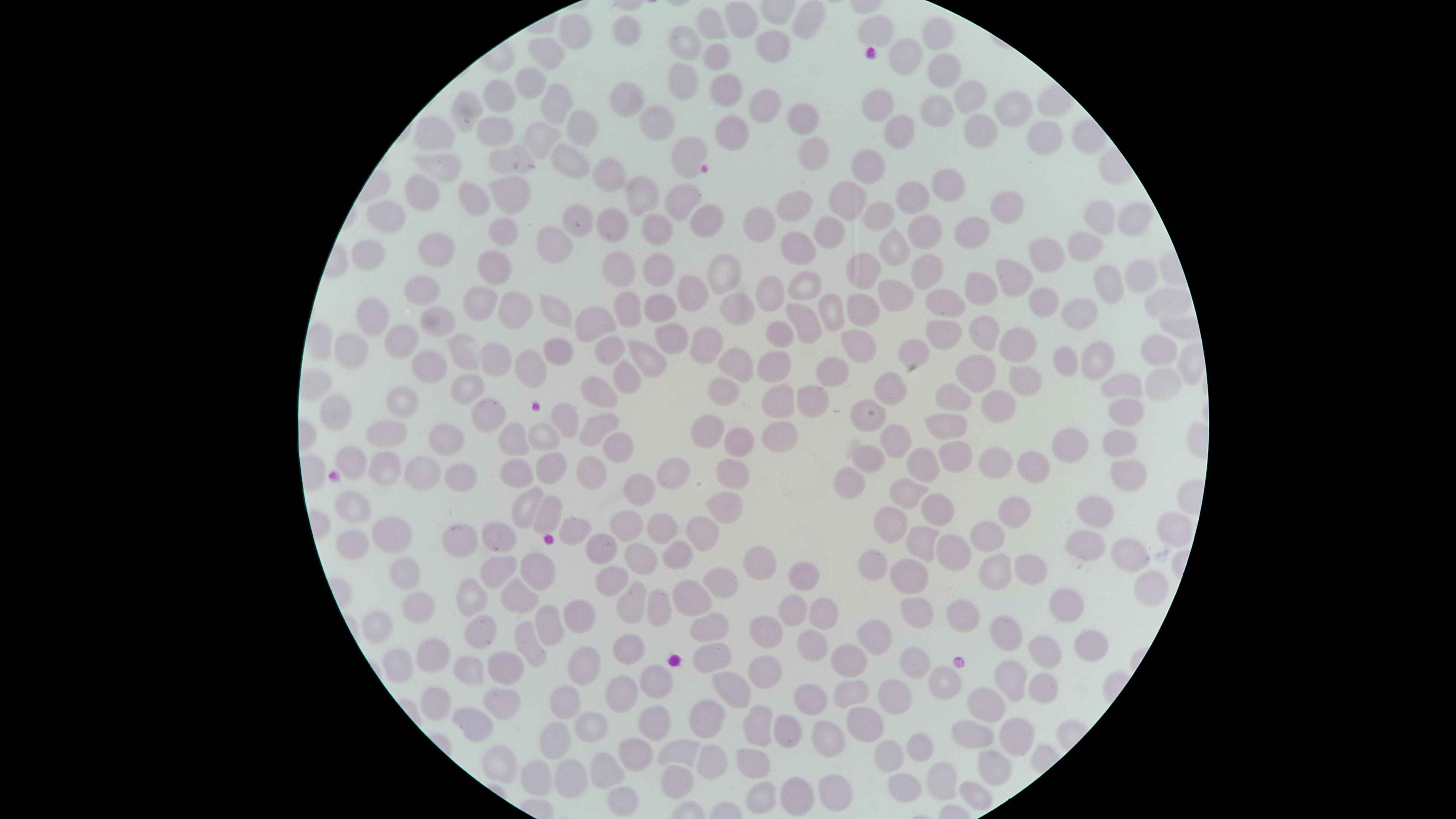
Approximate marker points as {x, y} in pixels. Uninfected red blood cells: {804, 22}, {744, 26}, {715, 29}, {576, 30}, {936, 30}, {879, 32}, {630, 36}, {682, 44}, {776, 48}, {547, 56}, {716, 58}, {903, 59}, {684, 74}, {940, 76}, {530, 81}, {726, 87}, {883, 97}, {965, 99}, {502, 100}, {631, 103}, {759, 105}, {558, 106}, {934, 106}, {1007, 110}, {470, 111}, {799, 115}, {660, 117}, {576, 123}, {491, 128}, {901, 128}, {740, 132}, {980, 132}, {432, 133}, {541, 133}, {1046, 137}, {814, 143}, {508, 153}, {691, 154}, {567, 158}, {440, 162}, {873, 169}, {612, 172}, {951, 186}, {510, 189}, {428, 194}, {640, 195}, {916, 197}, {477, 199}, {851, 199}, {680, 202}, {792, 203}, {1009, 206}, {390, 213}, {881, 213}, {580, 216}, {1095, 220}, {1130, 221}, {705, 222}, {652, 224}, {917, 226}, {611, 227}, {754, 227}, {971, 232}, {834, 235}, {506, 238}, {798, 238}, {1090, 241}, {893, 245}, {553, 247}, {419, 248}, {1046, 250}, {363, 251}, {492, 265}, {616, 268}, {656, 268}, {1140, 269}, {720, 270}, {862, 270}, {926, 275}, {1017, 276}, {808, 281}, {1116, 281}, {428, 285}, {693, 290}, {986, 290}, {769, 293}, {893, 295}, {1045, 301}, {1156, 301}, {661, 303}, {476, 304}, {734, 307}, {555, 308}, {830, 308}, {379, 309}, {629, 309}, {943, 309}, {1084, 309}, {862, 311}, {513, 312}, {807, 316}, {589, 318}, {441, 322}, {944, 329}, {982, 332}, {778, 335}, {672, 336}, {1010, 339}, {608, 342}, {395, 344}, {706, 344}, {352, 346}, {566, 346}, {858, 349}, {917, 352}, {459, 353}, {650, 354}, {1146, 355}, {497, 356}, {1064, 357}, {1098, 360}, {432, 362}, {740, 365}, {778, 365}, {530, 366}, {835, 370}, {975, 371}, {1028, 372}, {626, 376}, {1162, 379}, {884, 381}, {1125, 388}, {604, 390}, {727, 390}, {465, 392}, {779, 394}, {407, 397}, {813, 400}, {947, 400}, {335, 406}, {997, 406}, {1126, 407}, {864, 414}, {488, 416}, {564, 418}, {948, 421}, {598, 423}, {708, 428}, {777, 428}, {392, 432}, {445, 433}, {538, 434}, {894, 435}, {746, 437}, {1117, 440}, {514, 445}, {1074, 446}, {615, 450}, {868, 454}, {955, 456}, {925, 457}, {350, 459}, {734, 462}, {990, 462}, {555, 465}, {383, 466}, {1044, 466}, {1125, 466}, {458, 470}, {419, 472}, {587, 472}, {517, 474}, {671, 478}, {854, 482}, {638, 489}, {901, 493}, {525, 502}, {353, 503}, {729, 503}, {943, 508}, {1100, 510}, {1010, 513}, {545, 515}, {624, 523}, {1169, 524}, {704, 525}, {892, 525}, {662, 529}, {390, 530}, {986, 534}, {503, 537}, {1075, 540}, {458, 541}, {357, 542}, {923, 545}, {604, 548}, {960, 549}, {675, 554}, {1127, 557}, {638, 559}, {756, 559}, {1029, 564}, {875, 565}, {494, 566}, {997, 568}, {541, 569}, {403, 571}, {802, 571}, {908, 573}, {611, 578}, {719, 583}, {1148, 587}, {693, 593}, {469, 597}, {522, 599}, {1063, 602}, {416, 604}, {629, 605}, {914, 607}, {652, 608}, {795, 613}, {821, 615}, {957, 617}, {568, 618}, {717, 623}, {370, 626}, {545, 626}, {480, 629}, {877, 629}, {764, 632}, {1012, 633}, {626, 640}, {1085, 640}, {527, 642}, {809, 642}, {435, 645}, {1043, 651}, {852, 658}, {709, 659}, {916, 660}, {402, 664}, {579, 664}, {466, 668}, {504, 671}, {763, 676}, {655, 681}, {1042, 681}, {940, 682}, {1004, 682}, {855, 684}, {734, 689}, {619, 694}, {897, 695}, {806, 698}, {496, 702}, {982, 703}, {564, 704}, {434, 708}, {713, 714}, {650, 721}, {862, 721}, {792, 722}, {473, 725}, {757, 725}, {592, 726}, {978, 730}, {1019, 732}, {832, 734}, {555, 737}, {914, 746}, {676, 749}, {632, 753}, {880, 755}, {713, 759}, {752, 760}, {498, 764}, {606, 765}, {996, 766}, {569, 776}, {940, 776}, {532, 778}, {670, 787}, {832, 787}, {897, 788}, {974, 789}, {799, 790}, {761, 797}, {620, 801}. Single field of view. Circular visible region. Presence: no malaria parasites identified. Thin smear of blood. Giemsa stain. Image is 1456×819 pixels. Smartphone photograph through the microscope eyepiece.